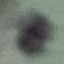

malaria status = uninfected
capture = smartphone camera at the microscope eyepiece
preparation = thin blood smear
stain = Giemsa
image type = automatically extracted cell patch, resized to 64 × 64 pixels